Classify this cell by malaria status.
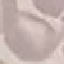
It is uninfected.

Summary:
  - Preparation: thin smear
  - Capture: smartphone through the microscope eyepiece
  - Stain: Giemsa
  - Image type: cell patch, automatically extracted from a larger field of view and resized to 64 × 64 pixels